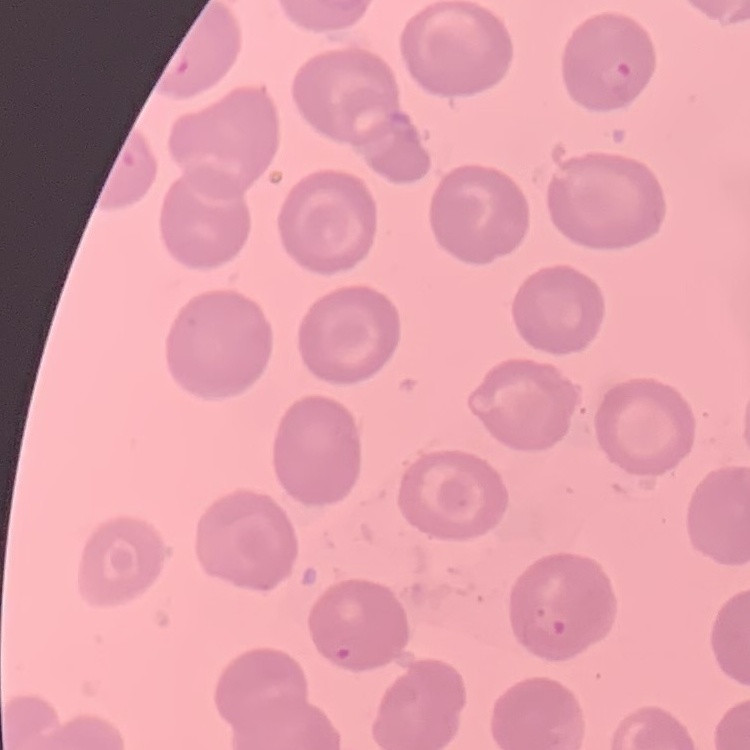
erythrocyte_morphology: no rouleaux formation
image_type: square crop of a larger photomicrograph
stain: Field's or Giemsa
preparation: thin blood smear